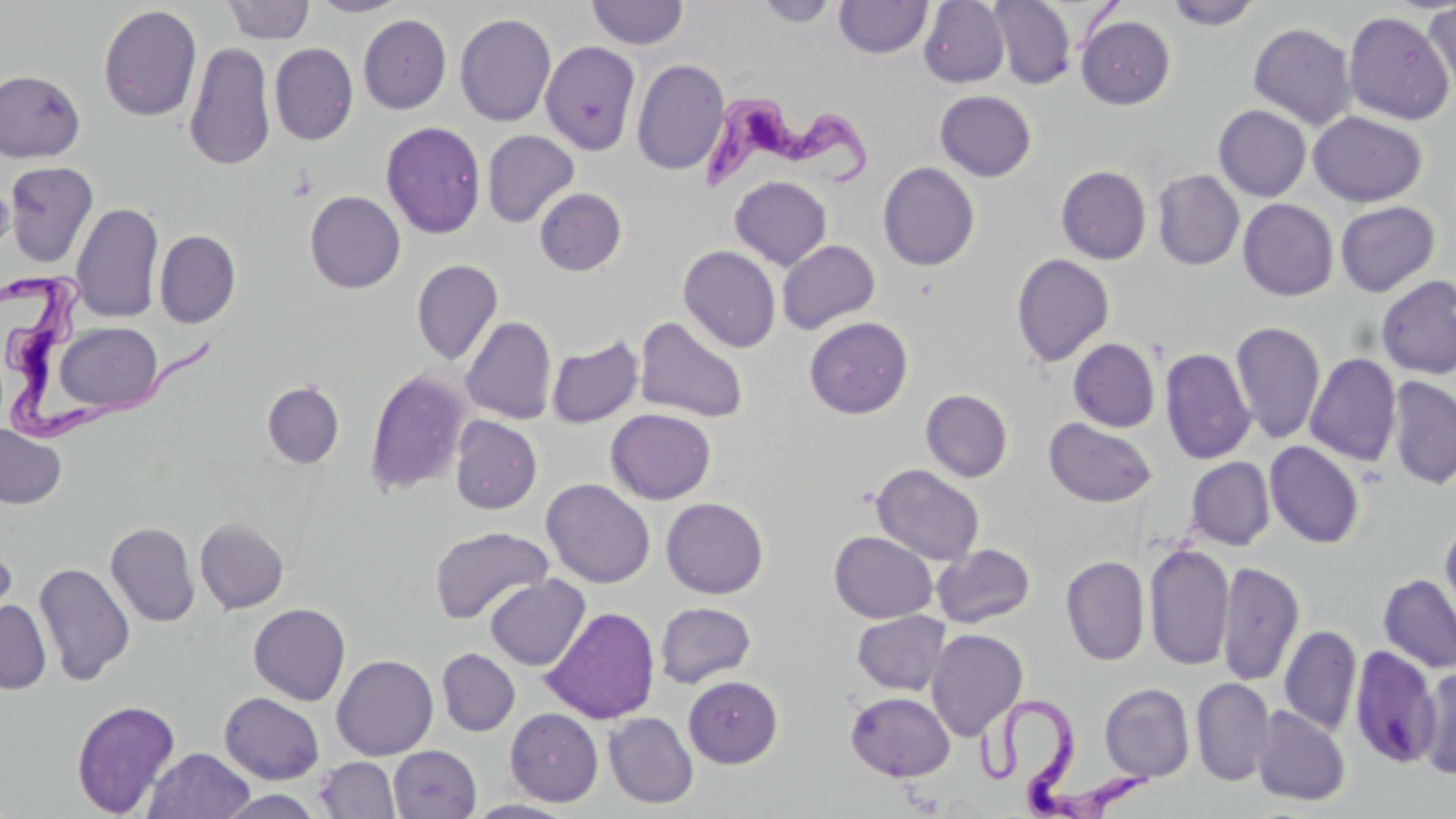
slide_level_diagnosis: Trypanosoma brucei
modality: optical microscopy
magnification: 1000x
trypanosoma_brucei_locations: 'approximate bounding boxes as (x1, y1, x2, y2) in pixels: (700, 93, 870, 198), (1, 273, 216, 444), (973, 692, 1152, 818)'
stain: May-Grünwald-Giemsa
field_of_view: single
preparation: thin blood smear
uninfected_red_blood_cell_locations: 'approximate bounding boxes as (x1, y1, x2, y2) in pixels: (307, 0, 412, 17), (754, 0, 841, 27), (834, 0, 933, 59), (918, 0, 1009, 88), (988, 0, 1076, 90), (220, 1, 315, 44), (586, 1, 689, 49), (1164, 1, 1263, 30), (1424, 1, 1456, 97), (98, 5, 202, 122), (1343, 11, 1454, 125), (455, 13, 556, 126), (358, 14, 451, 114), (1076, 15, 1176, 109), (1248, 22, 1355, 130), (541, 41, 641, 156), (184, 42, 276, 171), (269, 42, 358, 146), (632, 59, 730, 176), (0, 69, 86, 162), (934, 89, 1036, 181), (1213, 105, 1311, 201), (1308, 111, 1427, 206), (381, 121, 486, 239), (482, 130, 579, 228), (3, 161, 99, 268), (878, 162, 980, 271), (1056, 165, 1151, 265), (1152, 169, 1244, 270), (0, 176, 13, 260), (729, 176, 832, 270), (534, 187, 627, 276), (305, 190, 405, 293), (1237, 198, 1339, 301), (1335, 201, 1440, 296), (71, 202, 164, 323), (154, 230, 241, 328), (777, 239, 880, 334), (678, 245, 781, 352), (1011, 253, 1115, 368), (411, 259, 504, 365), (1375, 274, 1456, 380), (460, 315, 557, 424), (635, 315, 750, 424), (804, 316, 913, 419), (1230, 320, 1325, 444), (53, 321, 164, 415), (546, 336, 644, 428), (1068, 338, 1160, 432), (1159, 347, 1256, 465), (1305, 353, 1401, 466), (364, 368, 472, 497), (1386, 376, 1456, 489), (261, 380, 345, 469), (921, 389, 1013, 483), (605, 408, 716, 505), (450, 415, 542, 514), (1044, 417, 1158, 508), (0, 424, 67, 509), (1265, 441, 1364, 548), (1186, 456, 1275, 551), (870, 464, 985, 567), (541, 478, 655, 588), (661, 497, 768, 599), (1440, 516, 1456, 631), (196, 517, 290, 613), (106, 522, 200, 627), (429, 525, 553, 625), (829, 531, 937, 623), (0, 534, 18, 633), (1144, 542, 1233, 672), (933, 543, 1035, 629), (1061, 555, 1149, 665), (1217, 560, 1304, 687), (33, 561, 136, 685), (1378, 573, 1456, 673), (485, 575, 590, 671), (0, 599, 52, 694), (655, 601, 756, 688), (248, 603, 351, 706), (541, 606, 660, 725), (851, 610, 950, 695), (1279, 625, 1361, 735), (926, 628, 1028, 740), (1348, 645, 1440, 769), (437, 648, 520, 735), (332, 654, 438, 760), (1417, 666, 1456, 779), (683, 675, 783, 768), (1191, 677, 1275, 786), (1099, 683, 1195, 783), (219, 691, 325, 784), (845, 691, 955, 782), (71, 698, 181, 817), (1251, 705, 1351, 806), (505, 708, 603, 806), (603, 712, 698, 809), (388, 745, 481, 819), (144, 748, 255, 819), (315, 757, 400, 817), (213, 790, 326, 819), (464, 799, 579, 818)'
image_size: 1456×819 pixels